Outline each blood parasite and name the species.
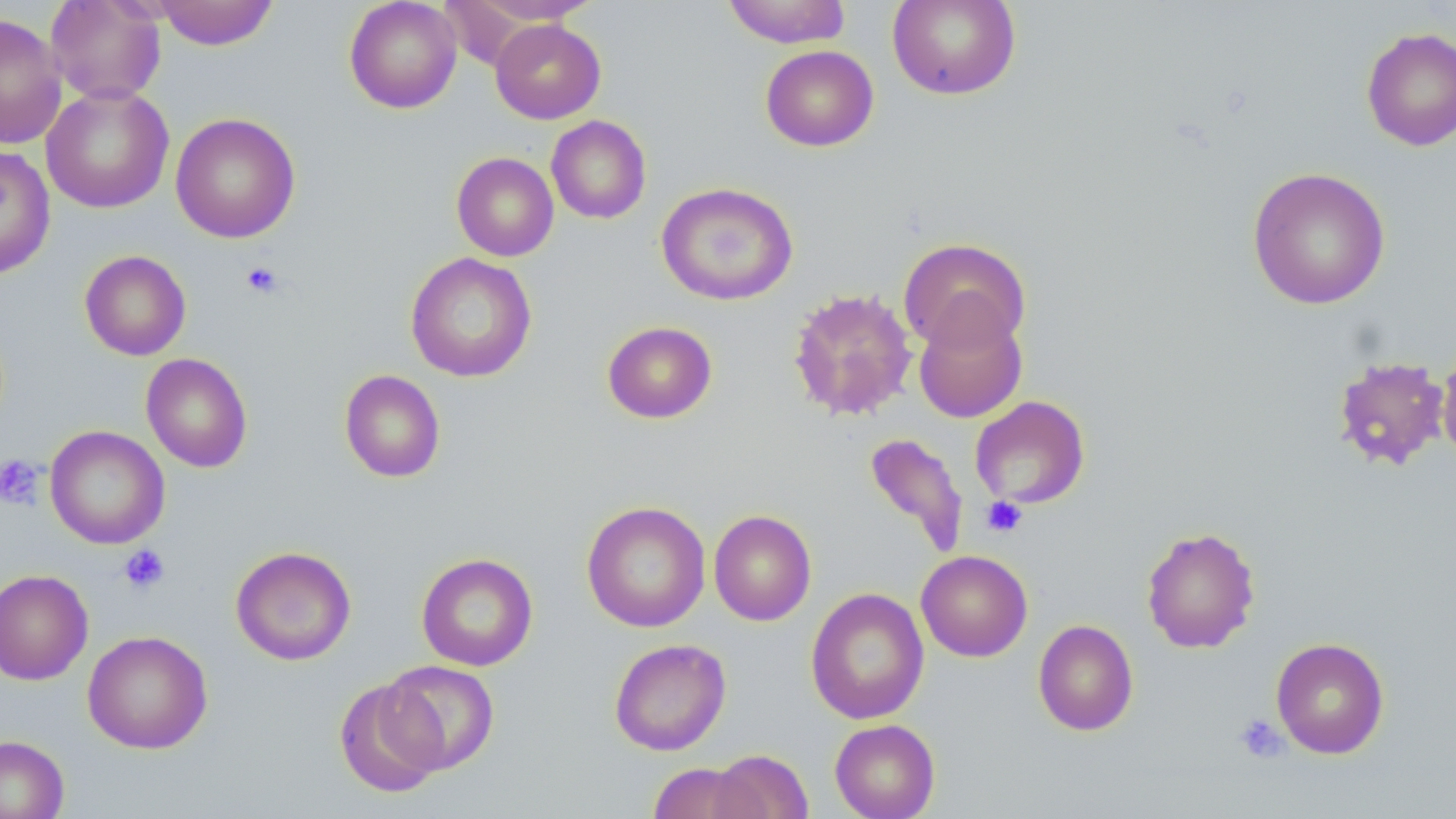
No blood parasites observed.

Approximate bounding boxes as (x1, y1, x2, y2) in pixels. Platelet locations: (241, 261, 285, 299), (0, 454, 45, 510), (981, 496, 1027, 537), (118, 544, 171, 595), (1234, 713, 1289, 763). Uninfected red blood cell locations: (45, 0, 166, 105), (152, 0, 279, 50), (344, 0, 462, 114), (464, 0, 603, 24), (722, 0, 852, 48), (887, 0, 1021, 100), (0, 13, 67, 150), (490, 18, 606, 124), (1361, 26, 1456, 152), (760, 45, 879, 151), (41, 83, 174, 213), (170, 112, 301, 243), (546, 115, 651, 224), (0, 145, 56, 279), (451, 152, 559, 261), (1247, 166, 1391, 310), (656, 182, 798, 306), (897, 237, 1032, 354), (79, 250, 191, 361), (405, 252, 537, 382), (788, 288, 918, 422), (913, 304, 1028, 424), (602, 320, 717, 423), (1435, 339, 1456, 464), (141, 353, 253, 473), (1331, 355, 1451, 473), (339, 369, 446, 483), (969, 395, 1091, 510), (45, 425, 170, 550), (863, 431, 969, 559), (581, 500, 711, 633), (709, 509, 816, 625), (1141, 526, 1261, 654), (230, 545, 356, 666), (916, 549, 1033, 662), (416, 552, 538, 671), (0, 569, 93, 685), (806, 587, 929, 725), (1033, 619, 1139, 736), (83, 630, 213, 754), (1270, 637, 1390, 759), (608, 638, 731, 756), (379, 660, 500, 775), (333, 677, 447, 800), (829, 718, 940, 819), (0, 735, 69, 819), (709, 749, 813, 819), (647, 762, 759, 819). Slide-level diagnosis: no evidence of blood parasites. Optical microscopy. One field of a larger specimen. Captured at 1000x magnification. Thin blood film. May-Grünwald-Giemsa stain. Image is 1456×819 pixels.